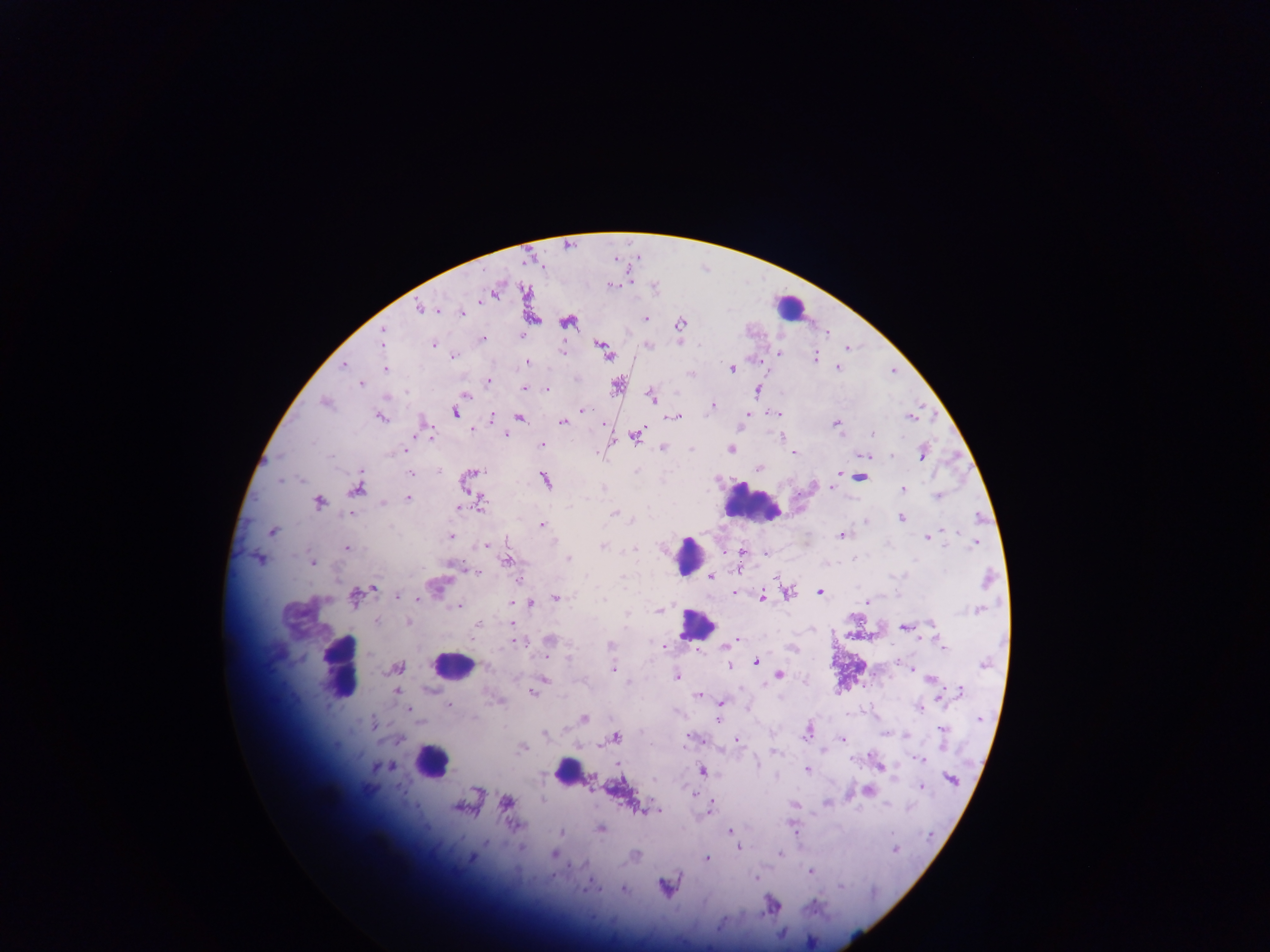

field of view = single
preparation = thick blood film
capture = mobile-phone photograph through a microscope
Plasmodium parasite locations = approximate centers as (x, y) in pixels: (612, 285), (482, 301), (419, 307), (462, 313), (645, 318), (567, 322), (680, 324), (383, 331), (522, 335), (482, 339), (382, 341), (433, 345), (647, 345), (601, 346), (605, 352), (561, 353), (780, 353), (453, 356), (815, 357), (527, 362), (343, 365), (732, 368), (837, 368), (386, 369), (691, 374), (488, 381), (361, 384), (617, 386), (524, 388), (547, 389), (758, 390), (465, 396), (651, 396), (325, 403), (713, 406), (582, 410), (455, 413), (776, 413), (380, 417), (491, 417), (675, 417), (909, 418), (519, 419), (563, 422), (837, 424), (472, 429), (873, 434), (428, 435), (505, 435), (636, 436), (782, 437), (541, 445), (663, 447), (731, 450), (395, 452), (793, 453), (923, 453), (866, 455), (891, 455), (759, 468), (439, 471), (473, 472), (410, 473), (839, 474), (860, 477), (545, 480), (279, 481), (832, 487), (357, 489), (903, 489), (937, 496), (408, 498), (319, 502), (481, 503), (384, 504), (459, 508), (351, 513), (615, 514), (901, 518), (632, 520), (542, 525), (944, 529), (272, 532), (841, 535), (450, 536), (927, 538), (974, 544), (486, 546), (602, 546), (347, 547), (635, 549), (740, 553), (744, 553), (765, 554), (568, 558), (258, 559), (506, 562), (313, 563), (451, 566), (477, 573), (703, 575), (712, 576), (988, 579), (435, 587), (374, 588), (735, 592), (787, 592), (819, 592), (398, 596), (762, 597), (354, 598), (417, 598), (557, 598), (604, 600), (529, 603), (866, 603), (459, 606), (977, 610), (659, 611), (627, 614), (377, 620), (408, 622), (477, 624), (512, 624), (932, 624), (904, 627), (550, 640), (734, 641), (518, 642), (730, 643), (610, 644), (661, 646), (942, 646), (792, 649), (568, 658), (756, 662), (983, 664), (397, 667), (729, 667), (910, 668), (613, 669), (779, 675), (676, 677), (544, 680), (932, 681), (397, 691), (960, 691), (533, 692), (697, 695), (498, 701), (720, 703), (449, 705), (920, 708), (410, 711), (583, 718), (718, 720), (980, 720), (373, 722), (942, 730), (808, 732), (544, 733), (885, 733), (615, 737), (689, 739), (400, 740), (737, 740), (842, 740), (523, 748), (775, 752), (920, 759), (878, 766), (389, 767), (807, 769), (702, 771), (951, 779), (921, 787), (868, 790), (691, 794), (506, 802), (827, 803), (795, 805), (886, 805), (909, 807), (457, 808), (710, 808), (645, 811), (653, 811), (601, 828), (729, 831), (561, 833), (487, 843), (737, 846), (894, 849), (553, 854), (780, 854), (636, 855), (471, 857), (707, 858), (810, 871), (755, 878), (664, 886), (840, 886), (590, 887), (623, 889)
country = Ghana
leukocyte locations = approximate centers as (x, y) in pixels: (790, 306), (753, 506), (688, 555), (696, 625), (452, 664), (341, 666), (431, 760), (566, 771)
image size = 1270×952 pixels